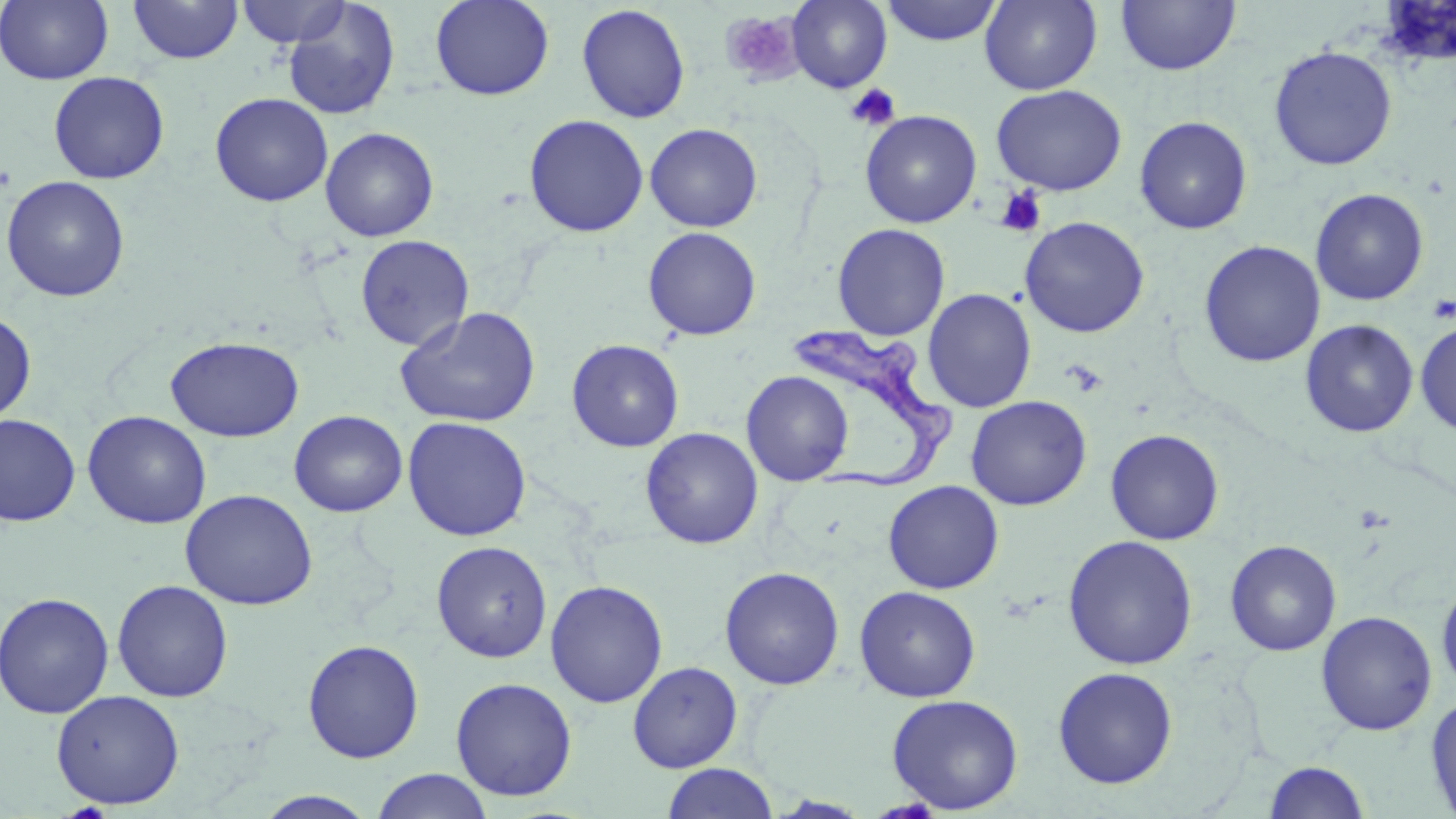
Approximate bounding boxes as (x1, y1, x2, y2) in pixels. Platelet locations: (720, 11, 801, 83), (845, 84, 901, 131), (996, 186, 1047, 237), (1427, 294, 1455, 323), (1063, 360, 1107, 397). Trypanosoma brucei locations: (791, 320, 959, 492). Uninfected red blood cell locations: (0, 0, 113, 85), (128, 0, 243, 64), (236, 0, 351, 48), (430, 0, 554, 101), (881, 0, 1003, 46), (979, 0, 1103, 95), (1115, 0, 1241, 76), (787, 1, 892, 92), (282, 2, 400, 120), (576, 4, 691, 124), (1268, 45, 1397, 171), (48, 71, 169, 184), (990, 84, 1127, 196), (210, 92, 333, 207), (860, 110, 982, 228), (523, 114, 649, 237), (1134, 116, 1253, 234), (645, 123, 762, 232), (320, 127, 439, 242), (1, 175, 130, 302), (1310, 188, 1429, 306), (1019, 216, 1150, 338), (832, 223, 950, 341), (642, 227, 761, 341), (355, 235, 474, 351), (1199, 240, 1325, 368), (922, 288, 1037, 413), (396, 307, 541, 429), (0, 312, 36, 425), (1300, 319, 1419, 438), (1415, 319, 1456, 437), (164, 335, 304, 442), (566, 338, 684, 452), (741, 370, 854, 486), (966, 395, 1092, 511), (82, 410, 212, 529), (289, 410, 408, 517), (0, 414, 81, 526), (402, 416, 531, 541), (641, 427, 763, 549), (1105, 428, 1225, 545), (883, 480, 1004, 594), (180, 489, 318, 610), (1062, 535, 1199, 670), (1224, 539, 1342, 656), (431, 540, 553, 663), (719, 566, 845, 690), (1436, 576, 1456, 696), (112, 579, 234, 702), (545, 579, 668, 708), (854, 586, 981, 703), (0, 591, 115, 719), (1316, 611, 1437, 736), (302, 639, 424, 764), (628, 661, 743, 773), (1053, 667, 1178, 789), (450, 677, 578, 801), (51, 689, 185, 809), (1425, 692, 1456, 819), (886, 694, 1023, 814), (1264, 760, 1370, 818), (661, 763, 780, 819), (370, 769, 493, 819), (254, 791, 380, 818). Slide-level diagnosis: Trypanosoma brucei. May-Grünwald-Giemsa-stained preparation. One field of a larger specimen. Thin blood film. Light microscopy. 1000x magnification. Image is 1456×819 pixels.